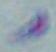

identification = Toxoplasma gondii
magnification = 1000x
modality = photomicrograph